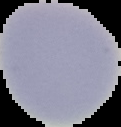
Summary:
  - Image type: segmented cell region with the area outside set to black
  - Image size: 121×127 pixels
  - Preparation: thin blood film
  - Result: no malaria parasites seen